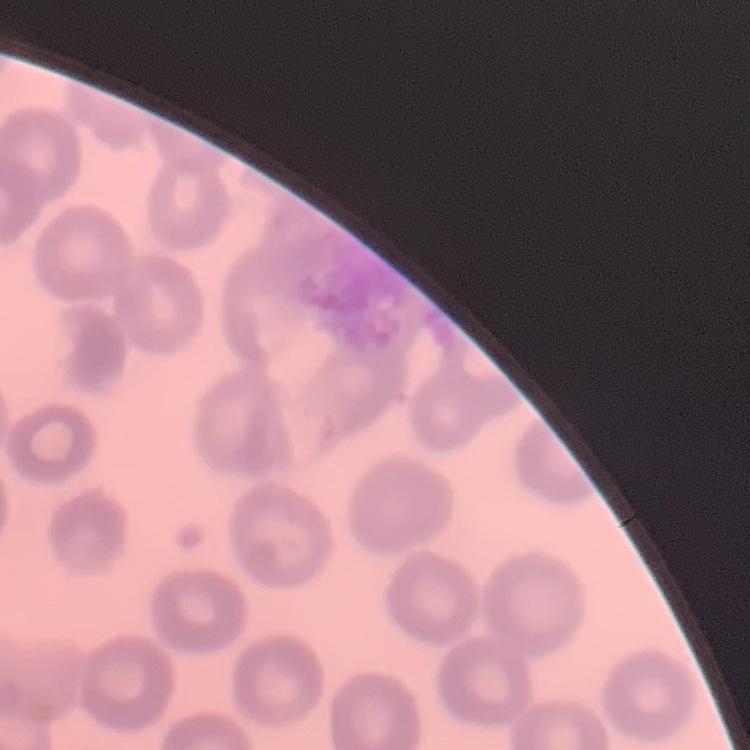 The erythrocytes show no rouleaux formation. Thin peripheral smear. Field's or Giemsa stain. Square crop of a larger photomicrograph.